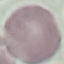

result: no malaria parasites seen
stain: Giemsa
image_type: automatically extracted cell patch, resized to 64 × 64 pixels
preparation: thin blood film
capture: smartphone through the microscope eyepiece